Outline each blood parasite and name the species.
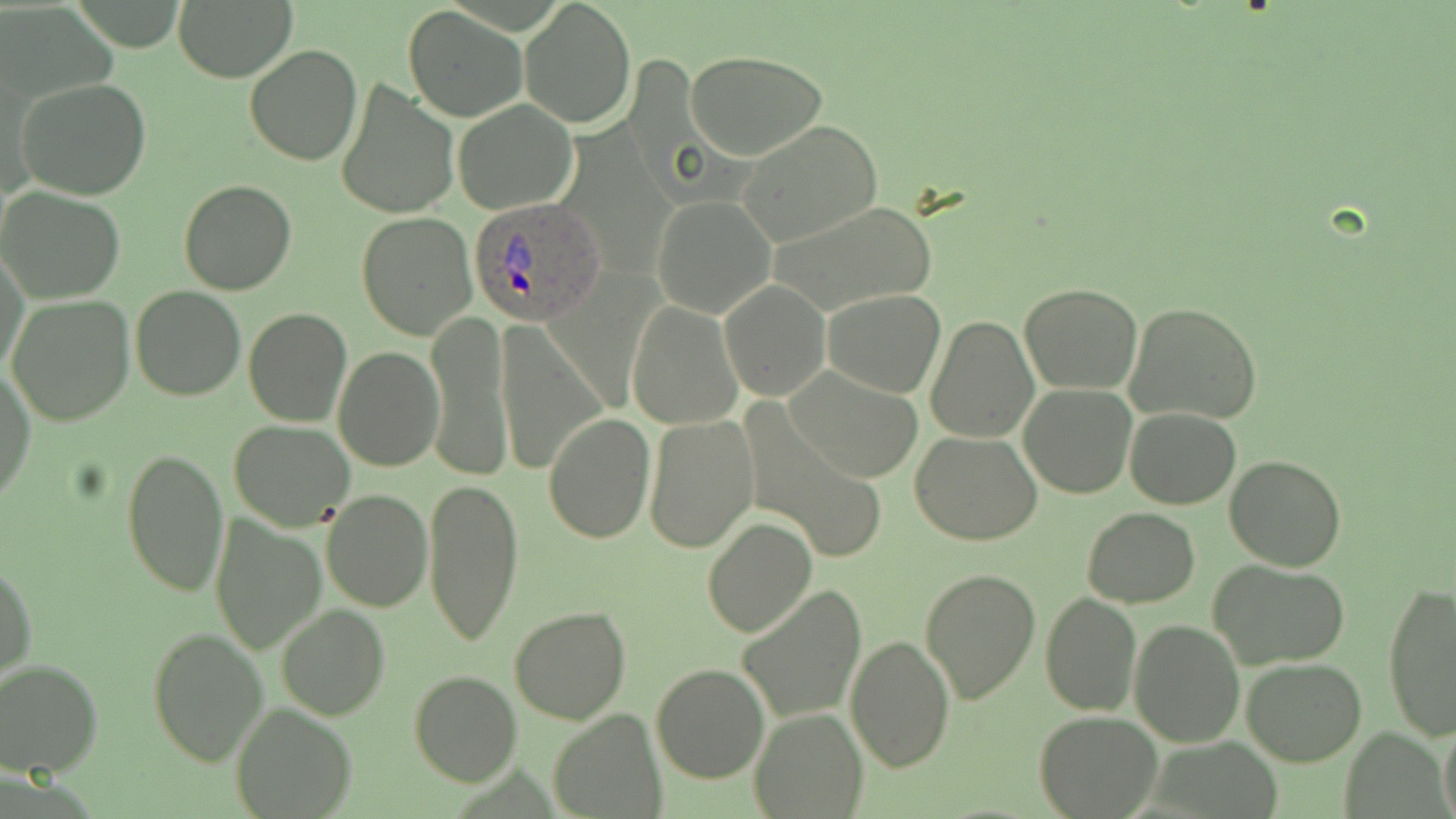
Approximate bounding boxes as (x1,y1)-(x2,y2) corner pairs in pixels.
Plasmodium ovale-infected red blood cells: (468,197)-(608,325).
No Plasmodium falciparum, Plasmodium malariae, Plasmodium vivax, Babesia divergens, or Trypanosoma brucei observed.

Uninfected red blood cell locations: (173,0)-(296,82), (520,1)-(636,129), (403,6)-(528,123), (244,45)-(362,166), (684,50)-(830,161), (334,78)-(459,221), (16,79)-(154,201), (453,101)-(578,214), (738,121)-(881,248), (179,180)-(299,296), (0,189)-(126,303), (651,195)-(776,317), (766,200)-(940,317), (355,212)-(478,340), (1,249)-(30,379), (720,281)-(829,400), (1020,283)-(1143,395), (130,285)-(245,401), (823,289)-(946,398), (6,294)-(133,426), (131,300)-(350,415), (1124,301)-(1263,424), (626,302)-(742,429), (243,308)-(351,425), (428,313)-(512,480), (925,315)-(1039,444), (495,319)-(608,478), (333,346)-(444,471), (0,367)-(35,503), (786,367)-(921,481), (1019,382)-(1138,498), (741,401)-(891,562), (1125,408)-(1242,509), (542,414)-(655,544), (643,415)-(760,553), (229,420)-(355,533), (911,431)-(1043,546), (119,449)-(229,598), (1225,455)-(1346,571), (422,474)-(524,649), (320,489)-(433,611), (1083,508)-(1200,607), (210,514)-(326,656), (702,518)-(816,638), (0,556)-(36,687), (1207,558)-(1350,670), (918,566)-(1039,705), (1381,581)-(1456,740), (736,584)-(866,724), (1040,591)-(1141,716), (276,603)-(390,720), (1043,603)-(1233,728), (509,606)-(631,725), (1129,619)-(1245,748), (145,625)-(269,768), (845,635)-(955,774), (0,659)-(102,777), (1241,659)-(1366,766), (651,663)-(770,783), (409,669)-(522,786), (231,701)-(357,818), (749,707)-(868,818), (1035,708)-(1161,818), (547,709)-(667,819), (1438,717)-(1456,819). Slide-level diagnosis: Plasmodium ovale. Thin blood film. Captured at 1000x magnification. May-Grünwald-Giemsa-stained preparation. Light microscopy. Image is 1456×819 pixels. One field of a larger specimen.